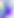
Summary:
  - Magnification: 400x
  - Modality: micrograph
  - Identification: Toxoplasma gondii